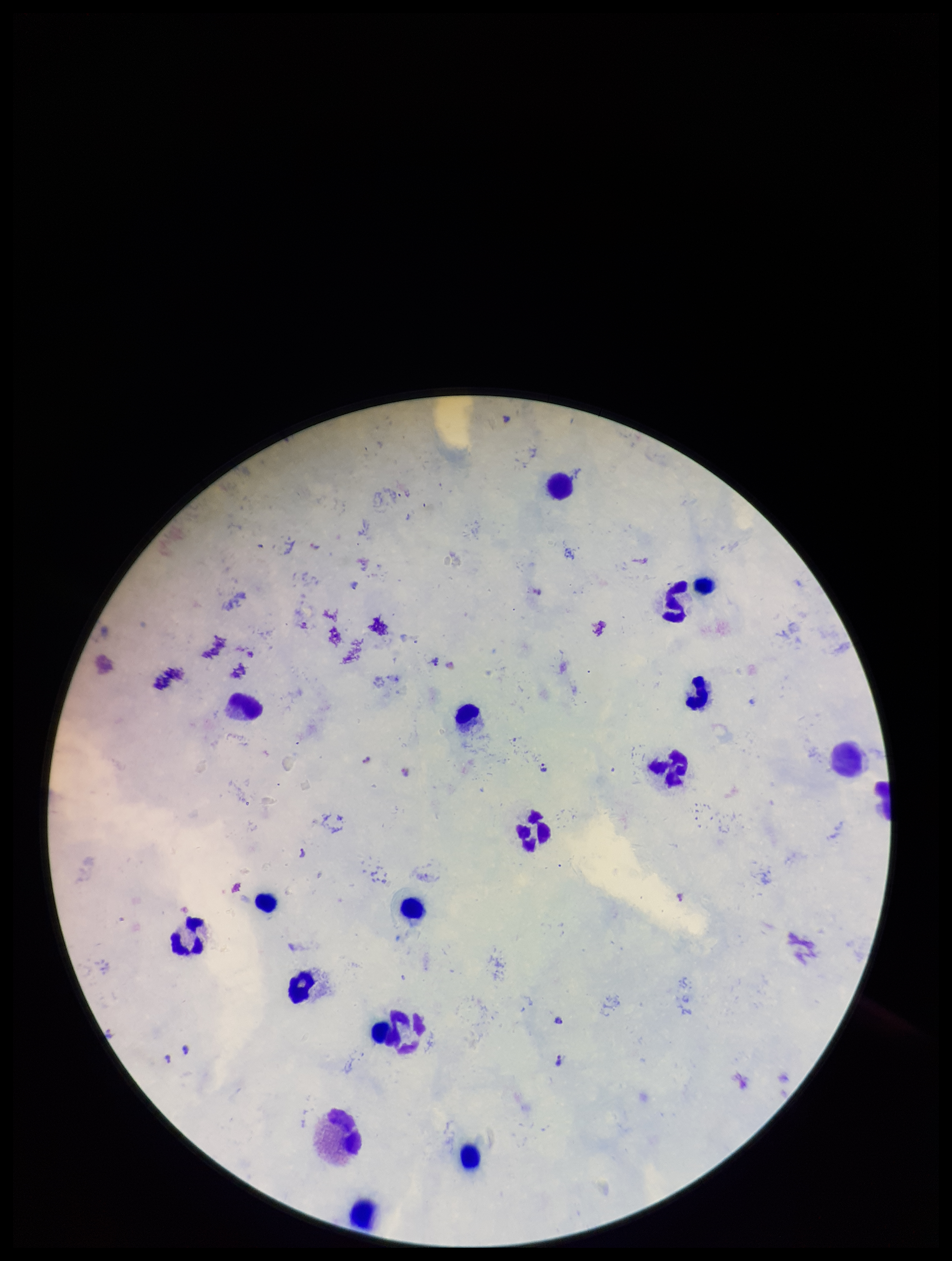

Plasmodium parasites: detected. Stained with Giemsa. Parasite count: 8. Species reported for this patient: Plasmodium falciparum. Image is 952×1261 pixels. Preparation: thick smear. One field from this slide. Smartphone photograph taken through the eyepiece of a microscope. Patient malaria status: infected. Leukocyte count: 18.